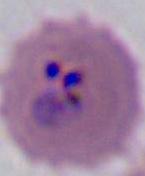

Summary:
  - Magnification: 400x or 1000x
  - Modality: photomicrograph
  - Identification: Plasmodium